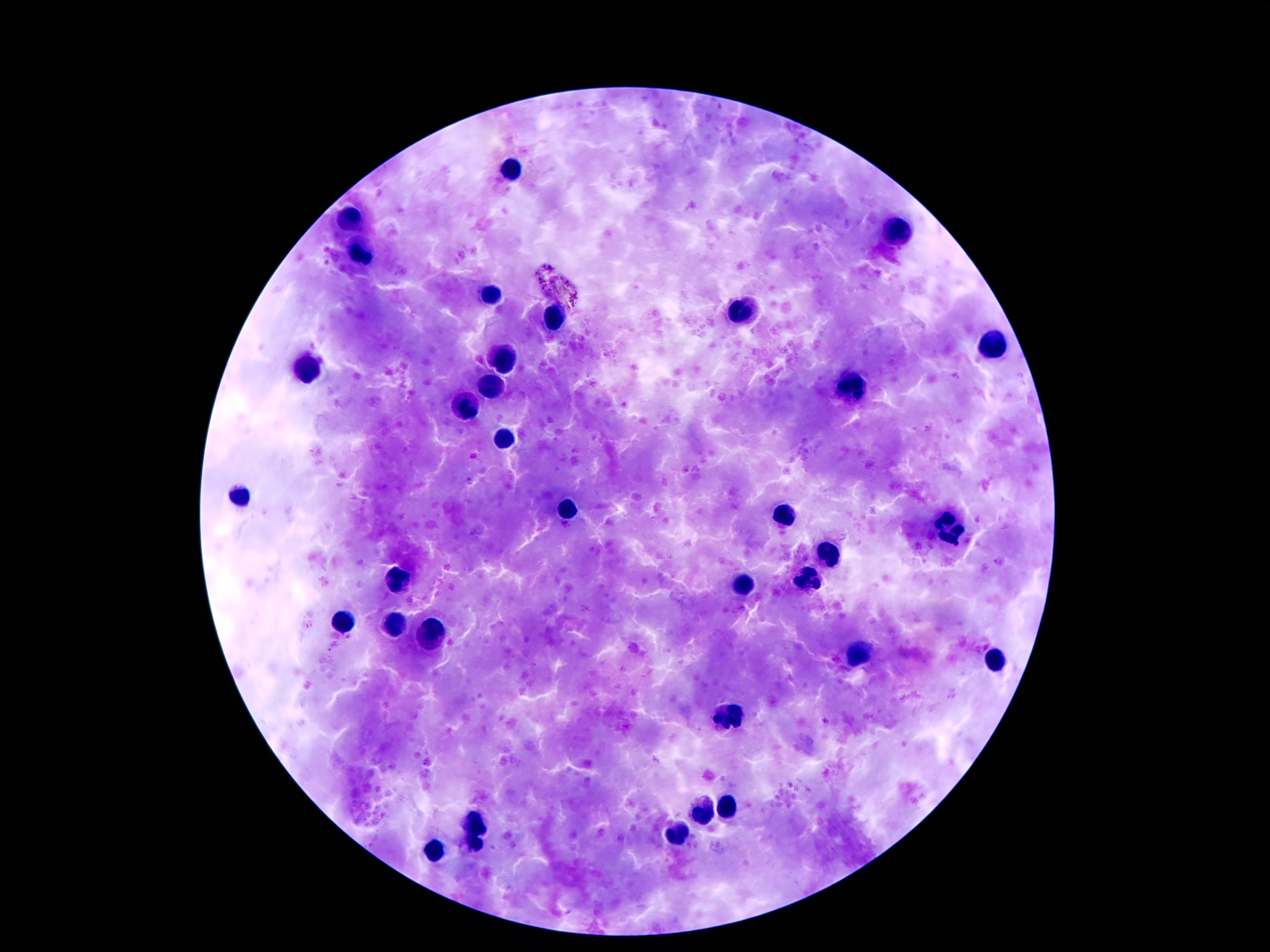

Approximate centers as (x, y) in pixels.
Summary:
  - Leukocyte locations: (508, 168), (352, 219), (897, 232), (361, 250), (494, 297), (744, 309), (555, 316), (993, 348), (502, 363), (309, 368), (848, 389), (492, 390), (467, 412), (502, 441), (238, 496), (567, 512), (782, 518), (948, 525), (828, 556), (395, 577), (807, 582), (743, 584), (340, 624), (393, 627), (430, 633), (860, 655), (995, 659), (727, 715), (727, 809), (700, 810), (475, 825), (676, 834), (475, 846), (434, 851)
  - Stain: Giemsa
  - Magnification: 100x
  - Patient malaria status: not infected
  - Capture: smartphone camera through the microscope eyepiece
  - Field of view: single
  - Image size: 1270×952 pixels
  - Preparation: thick blood film